Locate every blood parasite and identify its species.
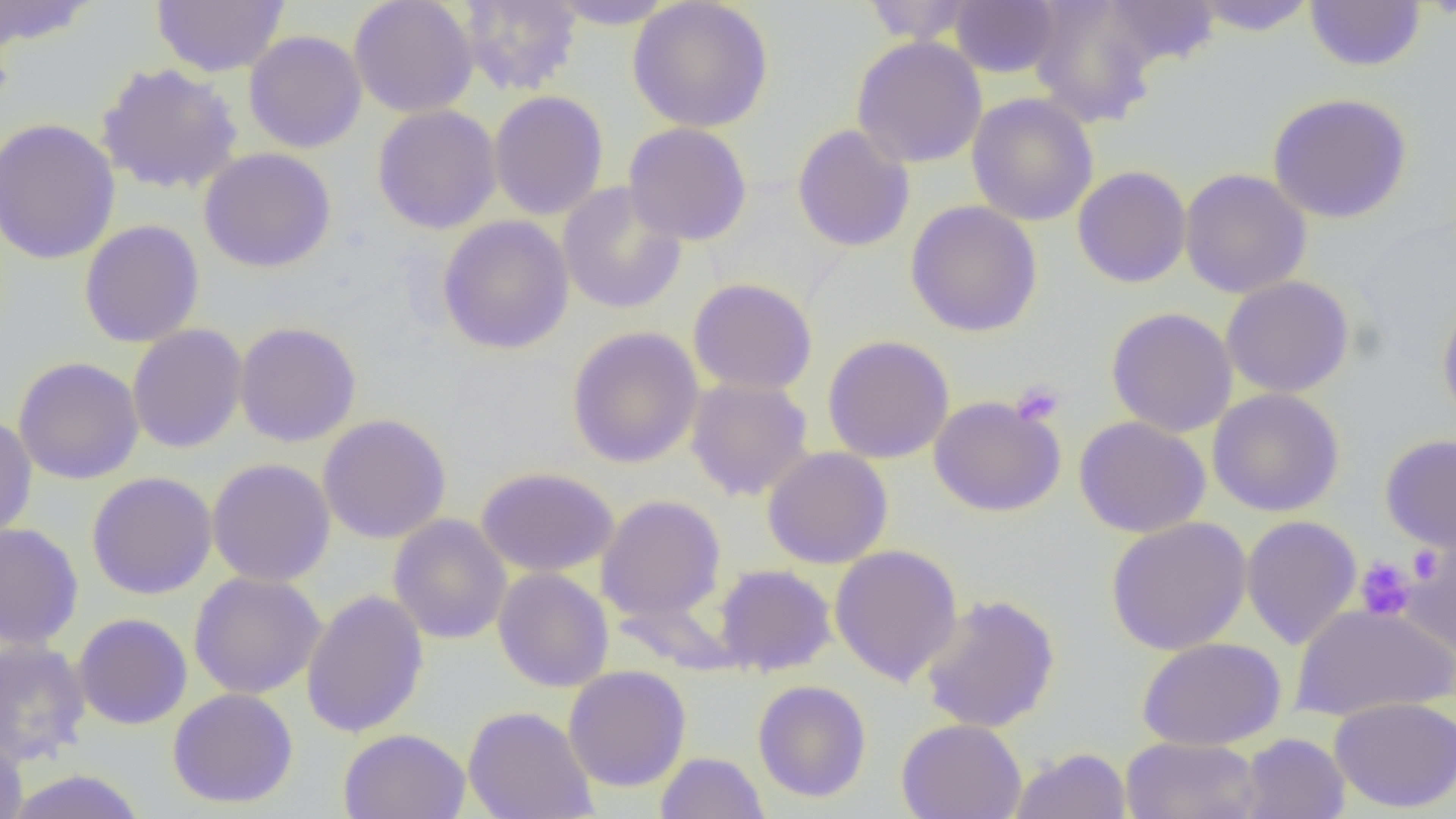

No blood parasites observed.

{
  "slide_level_diagnosis": "no evidence of blood parasites",
  "modality": "light microscopy",
  "magnification": "1000x",
  "uninfected_red_blood_cell_locations": "approximate bounding boxes as named x1/y1/x2/y2 corners in pixels: (x1=152, y1=0, x2=289, y2=77), (x1=458, y1=0, x2=582, y2=96), (x1=545, y1=0, x2=680, y2=29), (x1=628, y1=0, x2=774, y2=133), (x1=861, y1=0, x2=979, y2=44), (x1=949, y1=0, x2=1061, y2=78), (x1=1028, y1=0, x2=1159, y2=128), (x1=1100, y1=0, x2=1221, y2=70), (x1=1190, y1=0, x2=1318, y2=36), (x1=0, y1=1, x2=100, y2=50), (x1=349, y1=1, x2=479, y2=118), (x1=1305, y1=1, x2=1426, y2=72), (x1=244, y1=30, x2=367, y2=153), (x1=851, y1=36, x2=987, y2=169), (x1=96, y1=63, x2=244, y2=195), (x1=488, y1=90, x2=608, y2=220), (x1=1267, y1=92, x2=1413, y2=224), (x1=967, y1=93, x2=1099, y2=227), (x1=372, y1=105, x2=501, y2=234), (x1=0, y1=118, x2=121, y2=266), (x1=623, y1=122, x2=753, y2=246), (x1=792, y1=123, x2=915, y2=253), (x1=199, y1=147, x2=336, y2=273), (x1=1072, y1=166, x2=1192, y2=288), (x1=1179, y1=169, x2=1312, y2=299), (x1=557, y1=182, x2=687, y2=315), (x1=905, y1=200, x2=1043, y2=338), (x1=437, y1=215, x2=574, y2=355), (x1=79, y1=220, x2=205, y2=348), (x1=1221, y1=276, x2=1355, y2=398), (x1=688, y1=278, x2=817, y2=396), (x1=1437, y1=293, x2=1456, y2=429), (x1=1106, y1=307, x2=1237, y2=437), (x1=234, y1=321, x2=362, y2=447), (x1=127, y1=324, x2=248, y2=454), (x1=567, y1=326, x2=704, y2=468), (x1=822, y1=335, x2=955, y2=464), (x1=13, y1=357, x2=144, y2=485), (x1=685, y1=377, x2=814, y2=501), (x1=1207, y1=388, x2=1345, y2=517), (x1=1229, y1=389, x2=1351, y2=650), (x1=928, y1=396, x2=1066, y2=517), (x1=0, y1=413, x2=37, y2=540), (x1=318, y1=414, x2=452, y2=544), (x1=1074, y1=416, x2=1211, y2=538), (x1=1380, y1=433, x2=1456, y2=553), (x1=762, y1=447, x2=893, y2=569), (x1=207, y1=458, x2=336, y2=587), (x1=476, y1=466, x2=619, y2=577), (x1=86, y1=472, x2=217, y2=600), (x1=596, y1=495, x2=726, y2=623), (x1=388, y1=514, x2=512, y2=644), (x1=1106, y1=516, x2=1252, y2=655), (x1=1241, y1=516, x2=1362, y2=650), (x1=0, y1=523, x2=84, y2=650), (x1=1399, y1=536, x2=1456, y2=655), (x1=828, y1=543, x2=963, y2=686), (x1=715, y1=565, x2=837, y2=676), (x1=493, y1=568, x2=614, y2=693), (x1=188, y1=571, x2=326, y2=699), (x1=301, y1=589, x2=429, y2=739), (x1=919, y1=593, x2=1061, y2=733), (x1=1291, y1=602, x2=1456, y2=722), (x1=73, y1=613, x2=192, y2=730), (x1=1138, y1=637, x2=1286, y2=751), (x1=0, y1=639, x2=91, y2=767), (x1=563, y1=665, x2=692, y2=792), (x1=752, y1=680, x2=872, y2=803), (x1=167, y1=688, x2=299, y2=808), (x1=1328, y1=697, x2=1456, y2=814), (x1=463, y1=705, x2=598, y2=819), (x1=896, y1=718, x2=1027, y2=819), (x1=338, y1=728, x2=470, y2=819), (x1=0, y1=733, x2=28, y2=819), (x1=1238, y1=733, x2=1350, y2=819), (x1=1120, y1=736, x2=1264, y2=819), (x1=1009, y1=748, x2=1131, y2=819), (x1=655, y1=751, x2=770, y2=819), (x1=4, y1=768, x2=149, y2=818)",
  "image_size": "1456×819 pixels",
  "platelet_locations": "approximate bounding boxes as named x1/y1/x2/y2 corners in pixels: (x1=1010, y1=382, x2=1065, y2=426), (x1=1407, y1=546, x2=1444, y2=582), (x1=1354, y1=557, x2=1415, y2=621)",
  "field_of_view": "one of a larger specimen",
  "preparation": "thin blood film"
}